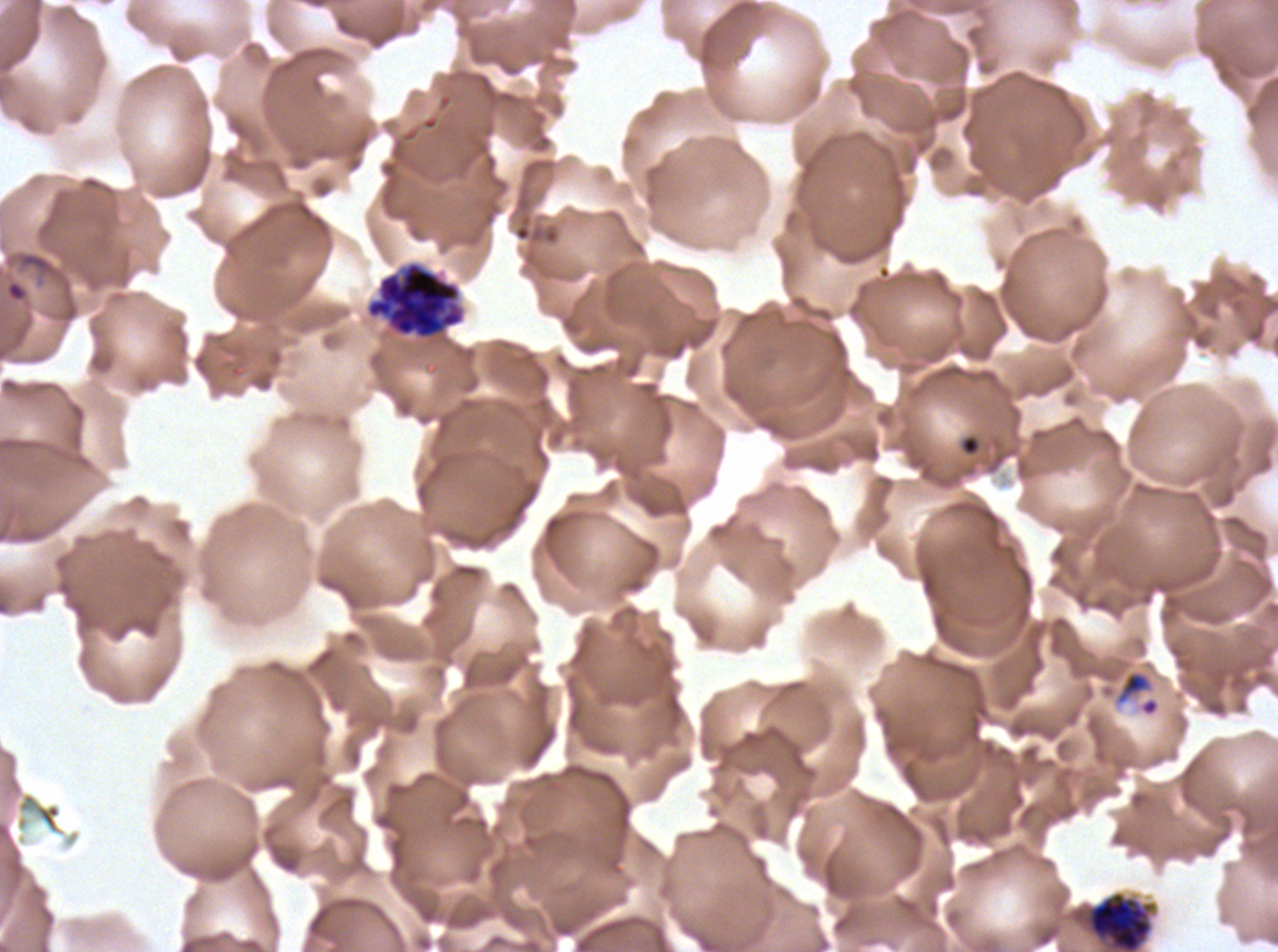

Approximate bounding boxes as (x1, y1, x2, y2) in pixels.
Summary:
  - Mid trophozoite locations: (1116, 670, 1152, 704)
  - Debris locations: (960, 434, 981, 457)
  - Late schizont locations: (365, 261, 466, 340)
  - Early schizont locations: (1086, 891, 1153, 951)
  - Ring locations: (6, 282, 25, 300)
  - Image size: 1278×952 pixels
  - Stain: Giemsa
  - Life-cycle stages observed: ring, mid trophozoite, early schizont, late schizont
  - Field of view: one sub-image of a larger composite
  - Specimen: ex-vivo P. falciparum culture from a patient in The Gambia, grown for 24 to 48 hours
  - Preparation: thin blood smear